State the preparation type.
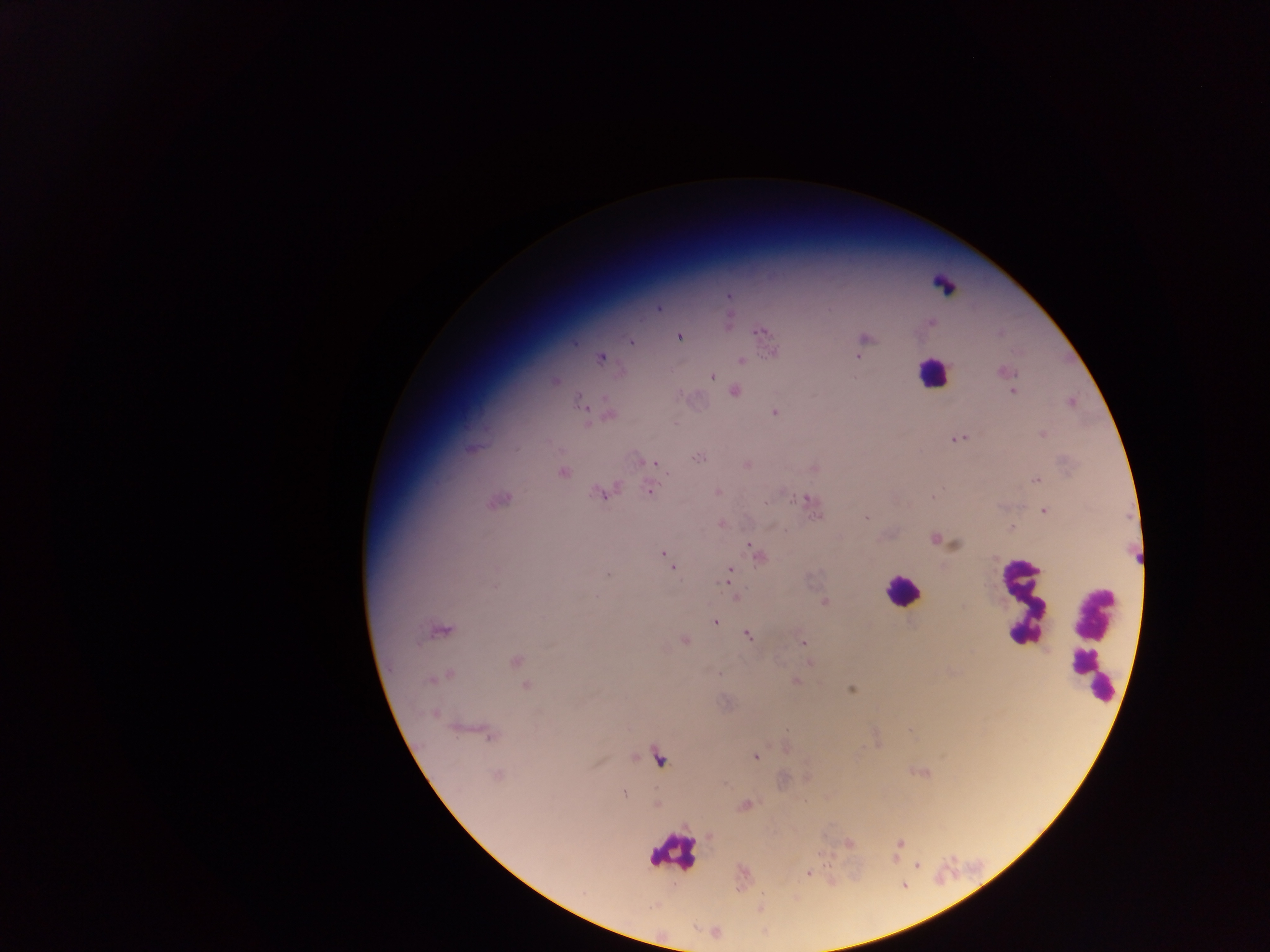
Thick blood film.

Approximate centers as (x, y) in pixels.
Summary:
  - Plasmodium parasite locations: (728, 296), (659, 307), (727, 321), (931, 322), (759, 331), (678, 336), (865, 338), (575, 342), (631, 342), (774, 352), (858, 356), (600, 357), (740, 360), (1004, 371), (711, 375), (555, 381), (734, 391), (1012, 391), (1071, 401), (581, 403), (774, 411), (609, 414), (1043, 434), (958, 438), (472, 447), (697, 456), (648, 462), (654, 463), (746, 465), (814, 468), (562, 472), (1035, 480), (650, 488), (717, 491), (601, 492), (933, 496), (498, 499), (804, 500), (765, 503), (1044, 510), (867, 517), (719, 523), (1010, 529), (935, 540), (750, 544), (663, 552), (757, 556), (667, 559), (672, 567), (730, 570), (607, 574), (728, 578), (735, 597), (824, 602), (715, 621), (439, 629), (746, 634), (685, 640), (803, 643), (515, 661), (445, 674), (795, 680), (525, 685), (851, 689), (434, 713), (486, 733), (755, 757), (496, 775), (623, 792), (655, 804), (744, 804), (847, 842), (900, 844), (807, 872)
  - Leukocyte locations: (944, 286), (931, 372), (902, 590), (1022, 601), (1094, 638), (658, 758), (672, 851)
  - Capture: mobile-phone photograph through a microscope
  - Country: Ghana
  - Field of view: single
  - Image size: 1270×952 pixels